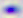 400x magnification. Micrograph. Toxoplasma gondii is shown.